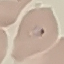

Result: malaria parasites identified. Acquired by smartphone through the microscope eyepiece. Giemsa stain. Thin blood smear. Automatically extracted cell patch, resized to 64 × 64 pixels.